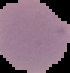
image size = 70×73 pixels
preparation = thin blood smear
result = no Plasmodium parasites detected
image type = segmented cell region with the area outside set to black